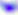

identification = Toxoplasma gondii
magnification = 400x
modality = photomicrograph